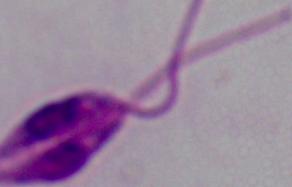
Summary:
  - Modality: photomicrograph
  - Identification: Leishmania
  - Magnification: 1000x